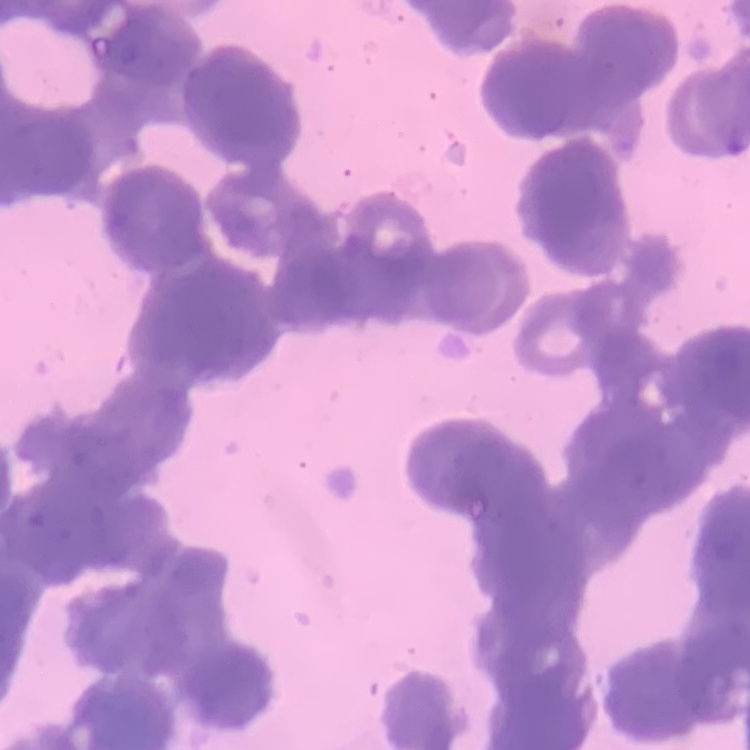
Summary:
  - Erythrocyte morphology: rouleaux formation
  - Stain: Field's or Giemsa
  - Preparation: thin blood film
  - Image type: one tile cut from a larger photomicrograph